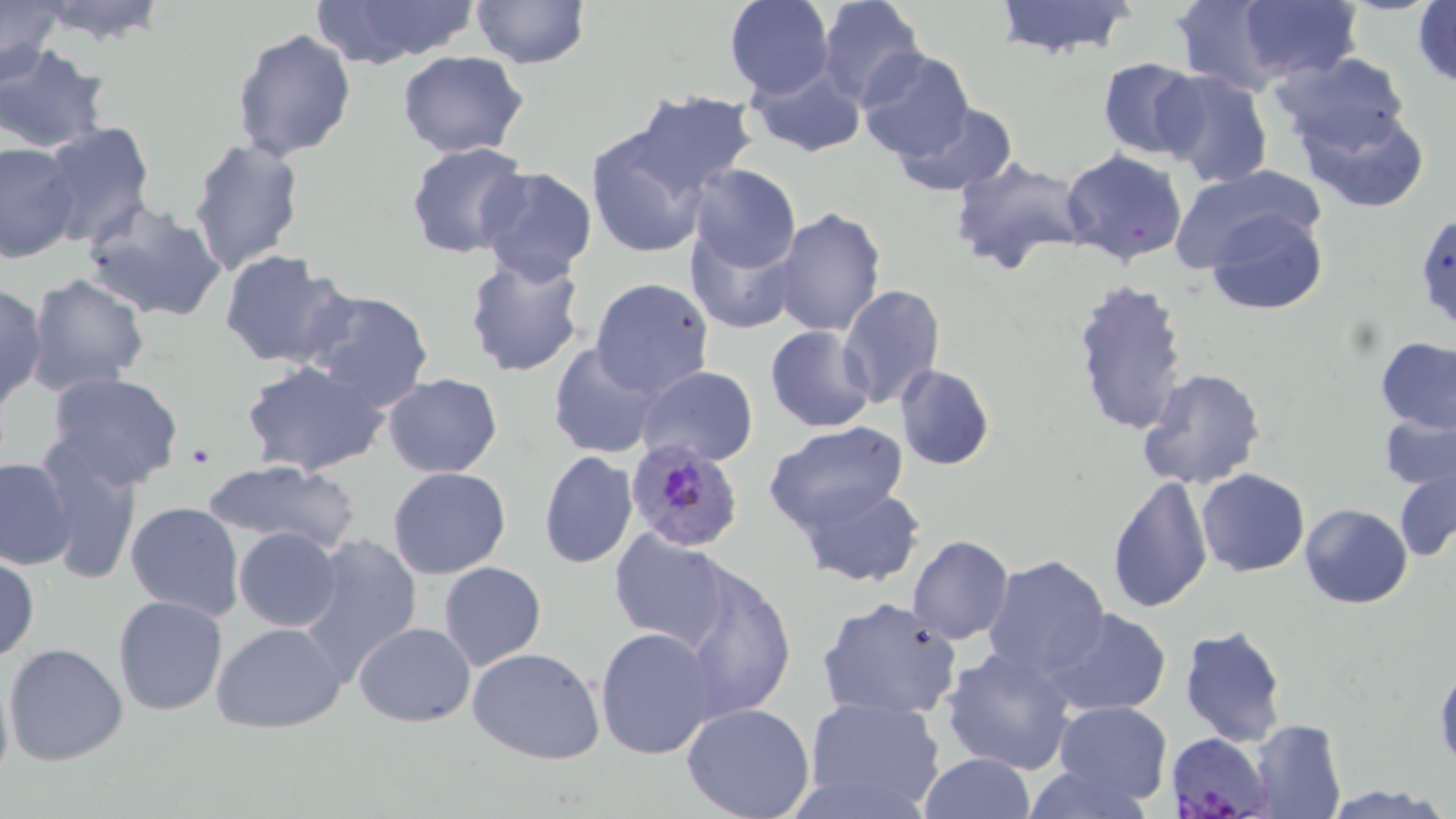 Approximate bounding boxes as (x1, y1, x2, y2) in pixels. Plasmodium falciparum-infected red blood cell locations: (622, 439, 745, 552), (1169, 735, 1272, 819). Uninfected red blood cell locations: (469, 0, 592, 70), (723, 0, 834, 99), (816, 0, 926, 106), (991, 0, 1139, 59), (1173, 0, 1291, 95), (1237, 0, 1363, 82), (0, 1, 64, 85), (29, 1, 173, 48), (311, 1, 481, 67), (1412, 1, 1456, 89), (231, 27, 356, 161), (0, 44, 110, 153), (856, 48, 974, 162), (396, 50, 530, 160), (1271, 51, 1412, 154), (1096, 56, 1204, 160), (746, 64, 868, 157), (1154, 71, 1275, 188), (625, 90, 760, 200), (887, 101, 1019, 197), (1297, 104, 1430, 212), (39, 122, 157, 249), (586, 128, 713, 260), (188, 138, 305, 273), (0, 141, 80, 263), (405, 142, 532, 261), (1059, 148, 1188, 265), (948, 155, 1089, 277), (476, 164, 598, 283), (685, 164, 801, 273), (1168, 164, 1324, 272), (78, 197, 230, 324), (769, 206, 886, 338), (1205, 208, 1330, 315), (1412, 211, 1456, 337), (687, 225, 799, 335), (462, 247, 590, 377), (219, 250, 353, 368), (25, 273, 151, 394), (589, 276, 714, 398), (1071, 279, 1192, 440), (0, 282, 47, 411), (836, 284, 947, 411), (300, 287, 436, 413), (765, 326, 877, 432), (1375, 337, 1456, 433), (548, 342, 666, 458), (241, 360, 389, 477), (893, 363, 996, 471), (636, 364, 759, 467), (1136, 367, 1266, 490), (44, 372, 187, 492), (382, 374, 503, 476), (1380, 411, 1456, 490), (762, 421, 909, 536), (37, 445, 143, 586), (538, 451, 638, 569), (0, 456, 75, 571), (202, 459, 362, 555), (388, 467, 511, 579), (1196, 468, 1309, 577), (1394, 468, 1456, 562), (1104, 474, 1214, 614), (796, 483, 925, 588), (124, 501, 245, 621), (1300, 503, 1413, 609), (610, 527, 735, 649), (234, 528, 342, 631), (294, 532, 422, 681), (906, 535, 1015, 645), (0, 553, 40, 662), (982, 554, 1112, 680), (674, 560, 798, 722), (438, 561, 548, 671), (111, 593, 229, 715), (815, 596, 963, 720), (1042, 605, 1173, 715), (211, 619, 348, 734), (352, 621, 474, 726), (1179, 624, 1289, 747), (595, 627, 720, 761), (4, 642, 128, 767), (465, 646, 606, 765), (939, 646, 1079, 775), (0, 660, 15, 792), (1433, 662, 1455, 770), (802, 696, 947, 816), (1053, 700, 1173, 806), (681, 702, 816, 819), (1249, 717, 1347, 819), (917, 753, 1037, 818), (1018, 763, 1153, 819). Platelet locations: (186, 443, 215, 469). Slide-level diagnosis: Plasmodium falciparum. One field of a larger specimen. Image is 1456×819 pixels. Thin blood smear. May-Grünwald-Giemsa stain. Optical microscopy. 1000x magnification.